Locate every Plasmodium parasite.
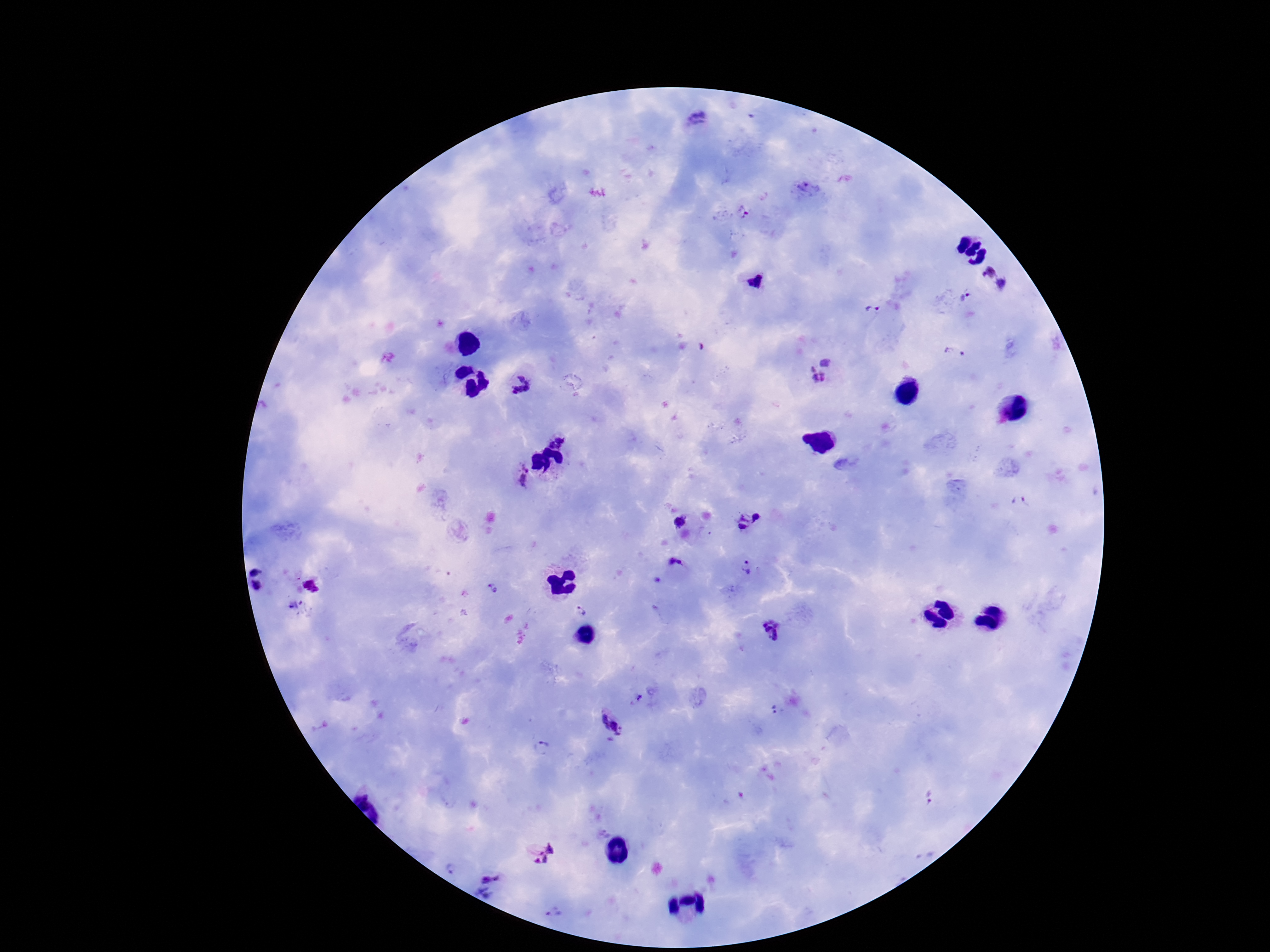

Approximate centers as {x, y} in pixels.
Plasmodium parasites: {695, 122}, {805, 191}, {742, 212}, {993, 280}, {755, 281}, {967, 298}, {872, 311}, {956, 354}, {819, 367}, {521, 387}, {562, 436}, {522, 477}, {1020, 503}, {682, 523}, {749, 523}, {748, 566}, {674, 568}, {260, 579}, {311, 585}, {492, 588}, {581, 612}, {770, 631}, {637, 698}, {774, 709}, {611, 727}, {543, 749}, {930, 798}, {541, 851}, {452, 869}, {487, 887}, {555, 911}.

image size = 1270×952 pixels
stain = Giemsa
field of view = one from this slide
capture = smartphone camera through the microscope eyepiece
preparation = thick blood smear
patient malaria status = infected
magnification = 100x